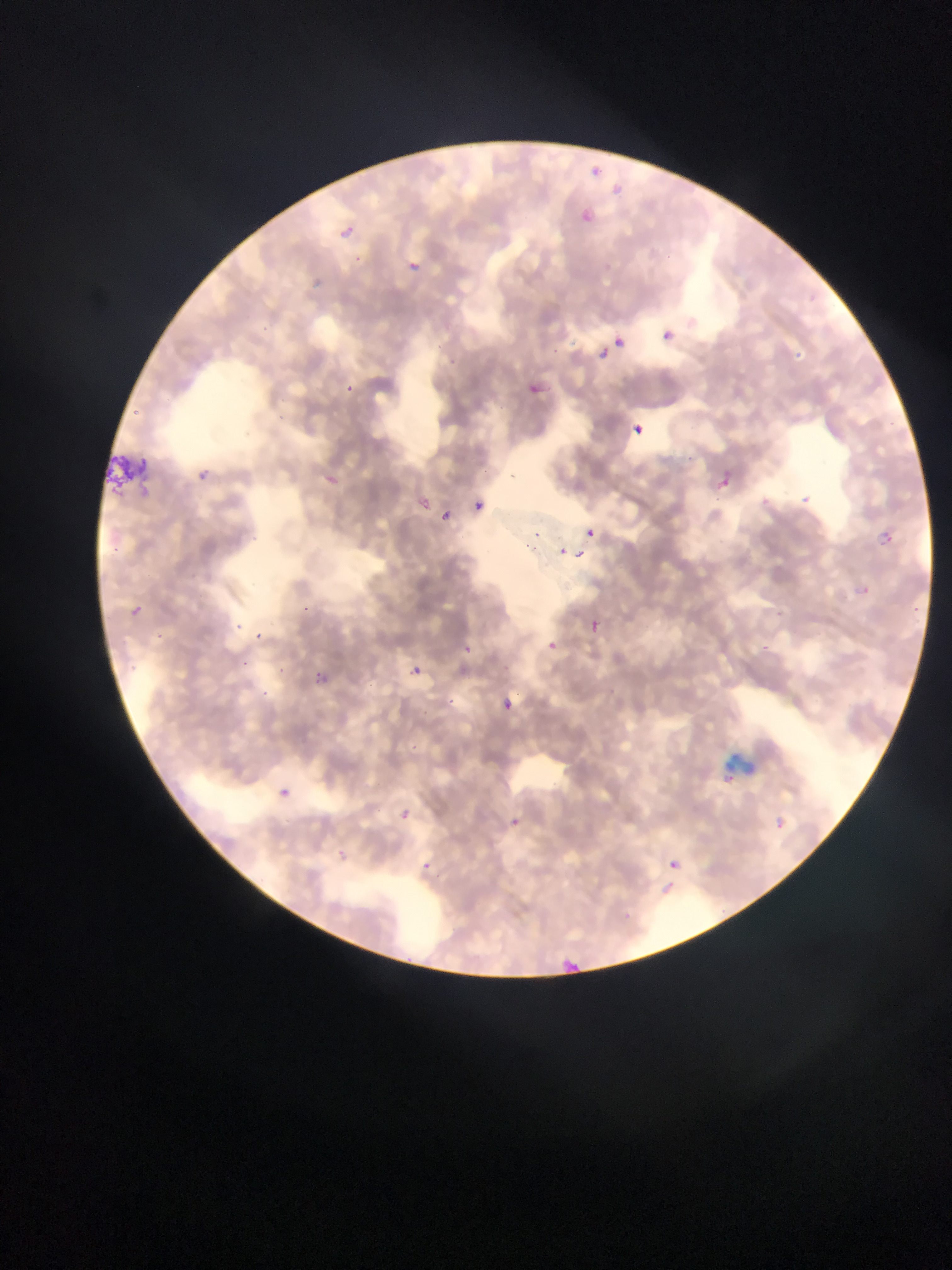

{
  "country": "Ghana",
  "field_of_view": "single",
  "capture": "mobile-phone photograph through a microscope",
  "image_size": "952×1270 pixels",
  "preparation": "thin blood film",
  "plasmodium_parasite_locations": "approximate bounding boxes as (left, top, right, bottom) in pixels: (585, 162, 604, 180), (576, 207, 598, 229), (334, 222, 361, 240), (397, 255, 419, 274), (662, 322, 686, 343), (611, 334, 628, 351), (594, 343, 615, 364), (522, 375, 555, 406), (632, 424, 645, 436), (194, 458, 218, 489), (715, 474, 732, 490), (411, 492, 436, 515), (799, 493, 815, 508), (800, 494, 811, 504), (471, 498, 488, 515), (437, 508, 454, 525), (583, 526, 598, 540), (556, 544, 570, 558), (573, 547, 587, 561), (127, 599, 149, 627), (583, 616, 604, 638), (251, 630, 270, 642), (540, 635, 562, 656), (756, 642, 771, 656), (407, 663, 425, 680), (307, 666, 336, 694), (495, 695, 518, 717), (718, 768, 739, 789), (272, 785, 293, 803), (392, 808, 419, 835), (498, 812, 526, 835), (768, 814, 790, 834), (327, 844, 351, 865), (659, 850, 689, 881), (561, 948, 582, 966)"
}